Give the position of every Plasmodium parasite.
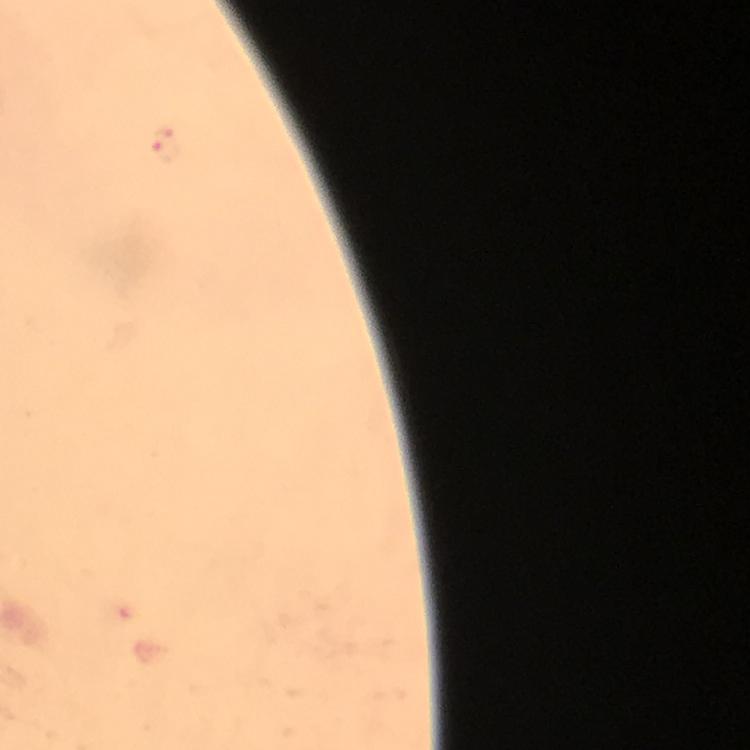

Approximate centers as [x, y] in pixels.
Plasmodium parasites: [165, 144].

immersion oil = used
preparation = thick blood film
magnification = 100x
capture = smartphone camera through the microscope
stain = Giemsa
image size = 750×750 pixels
context = from a malaria diagnostic workup
cropped from = a single field of view